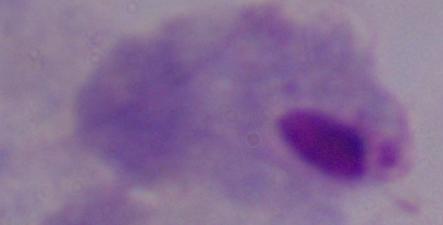

identification = trichomonad
magnification = 1000x
modality = micrograph